State which parasite is depicted.
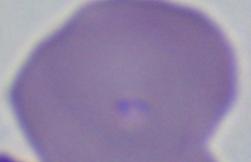

Babesia.

Micrograph. Captured at 1000x magnification.